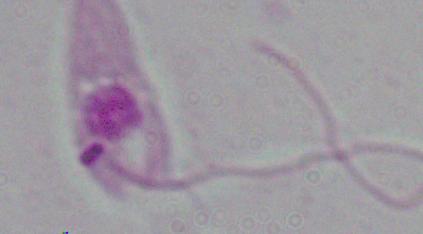
Summary:
  - Identification: Leishmania
  - Modality: micrograph
  - Magnification: 1000x